Name the parasite shown.
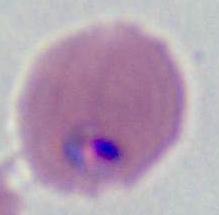
Plasmodium.

Captured at either 400x or 1000x magnification. Micrograph.